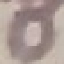

Summary:
  - Result: negative for malaria parasites
  - Preparation: thin blood film
  - Stain: Giemsa
  - Image type: automatically extracted cell patch, resized to 64 × 64 pixels
  - Capture: smartphone camera at the microscope eyepiece